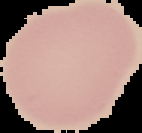

Summary:
  - Image size: 142×133 pixels
  - Image type: segmented cell region on a black background
  - Result: no Plasmodium parasites seen
  - Preparation: thin blood smear